Locate every Plasmodium parasite.
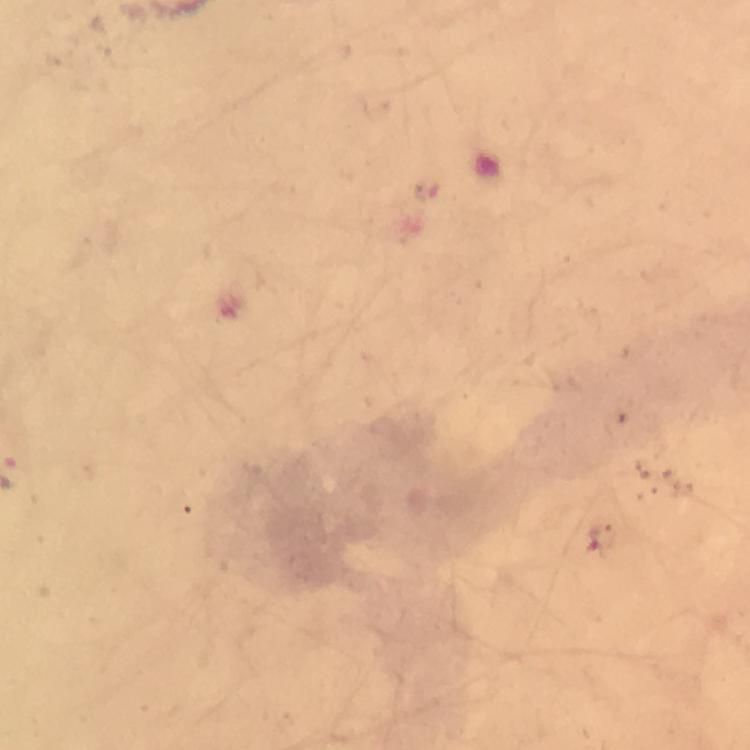

Approximate centers as (x, y) in pixels.
Plasmodium parasites: (602, 539).

Summary:
  - Preparation: thick blood smear
  - Stain: Giemsa
  - Capture: smartphone camera through the microscope
  - Immersion oil: used
  - Cropped from: a single field of view
  - Magnification: 100x
  - Context: from a diagnostic examination for malaria
  - Image size: 750×750 pixels